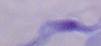

Micrograph. A trypanosome is shown. Captured at 1000x magnification.